Comment on the morphology of the red blood cells.
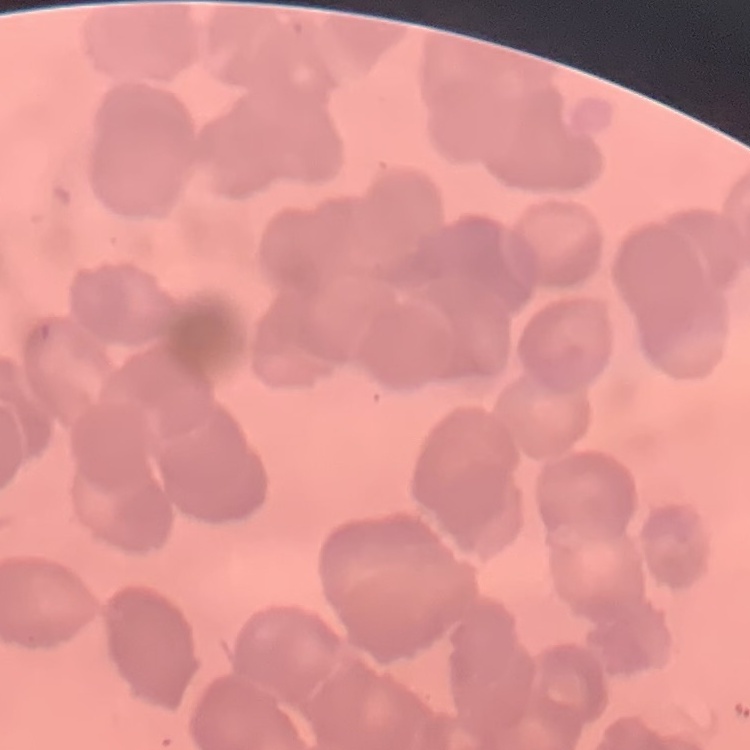
They show rouleaux formation.

Thin blood film. One tile cut from a larger photomicrograph. Stained with either Field's or Giemsa.